Name the blood parasite species.
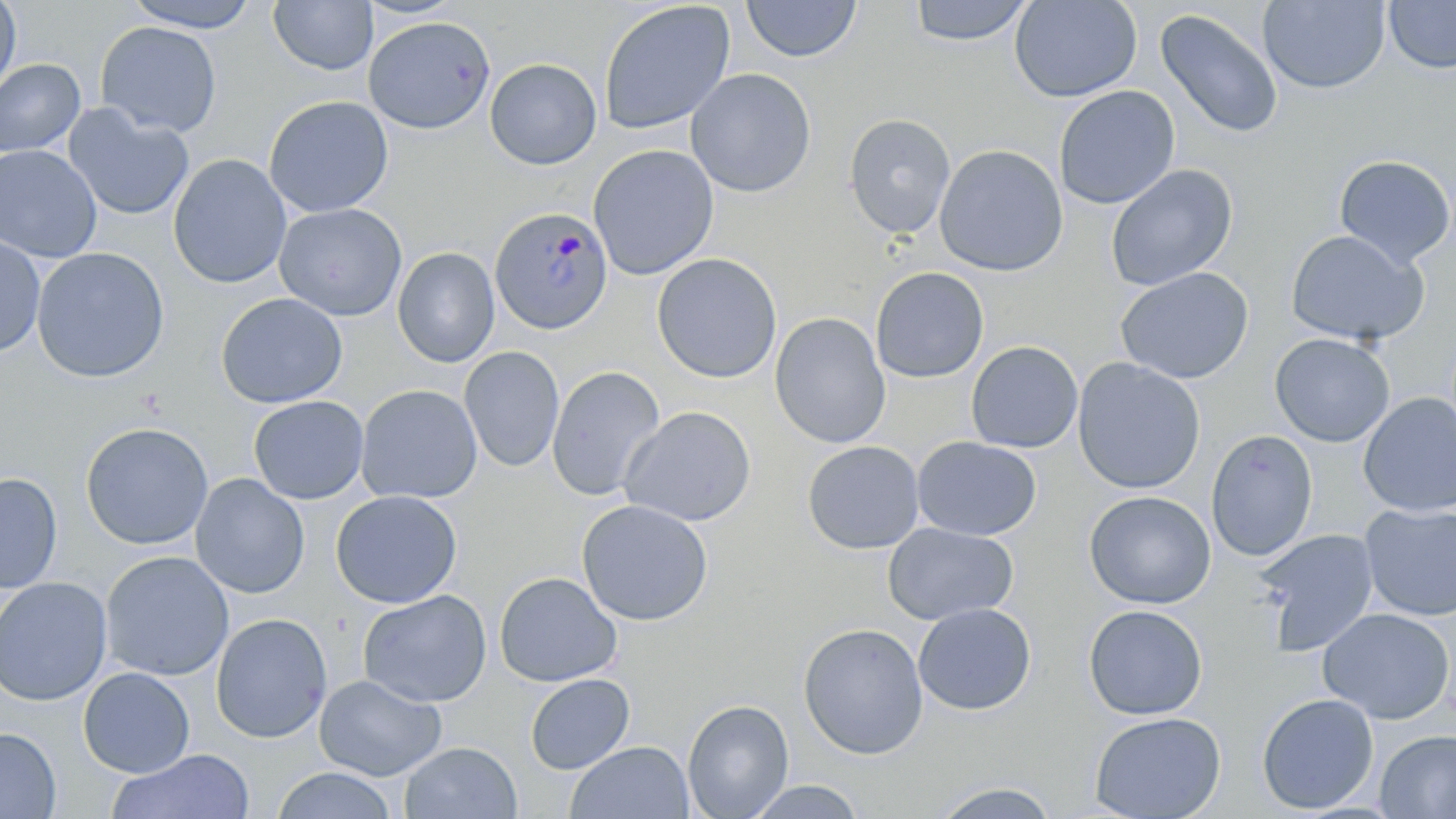

Plasmodium malariae.

Summary:
  - Coordinate format: approximate bounding boxes as [x1, y1, x2, y2] in pixels
  - Plasmodium malariae-infected red blood cell locations: [489, 207, 614, 336]
  - Uninfected red blood cell locations: [0, 0, 21, 97], [123, 0, 260, 31], [268, 0, 378, 76], [741, 0, 861, 63], [907, 0, 1034, 47], [1009, 0, 1142, 103], [598, 1, 736, 135], [1258, 1, 1391, 95], [1384, 1, 1456, 74], [1155, 8, 1284, 140], [362, 16, 495, 134], [95, 21, 222, 137], [0, 58, 85, 157], [485, 58, 602, 170], [685, 68, 817, 198], [1054, 85, 1180, 209], [264, 95, 394, 217], [63, 104, 195, 221], [843, 113, 956, 239], [0, 144, 102, 262], [588, 144, 719, 280], [934, 144, 1069, 276], [168, 154, 291, 289], [1334, 155, 1456, 268], [1105, 164, 1238, 291], [273, 203, 408, 321], [1285, 229, 1428, 346], [0, 235, 45, 357], [392, 246, 500, 368], [32, 247, 169, 382], [651, 253, 782, 383], [870, 266, 989, 383], [1115, 267, 1254, 384], [215, 292, 348, 409], [770, 312, 891, 448], [1269, 333, 1395, 447], [965, 341, 1083, 453], [459, 346, 564, 472], [1072, 358, 1206, 494], [547, 365, 665, 501], [356, 384, 483, 504], [1358, 393, 1456, 517], [248, 396, 369, 504], [619, 406, 757, 526], [80, 422, 214, 550], [1205, 429, 1318, 561], [912, 436, 1042, 542], [802, 441, 925, 554], [0, 473, 63, 593], [190, 474, 309, 598], [330, 490, 463, 608], [1083, 490, 1216, 609], [576, 499, 713, 627], [1360, 503, 1456, 621], [882, 522, 1018, 626], [1254, 529, 1380, 656], [100, 551, 234, 681], [494, 571, 622, 687], [0, 577, 113, 705], [357, 589, 492, 707], [913, 603, 1037, 716], [1083, 604, 1208, 720], [1317, 607, 1455, 724], [210, 613, 332, 744], [797, 622, 929, 759], [78, 667, 195, 777], [525, 673, 635, 774], [314, 674, 447, 781], [1256, 693, 1379, 814], [682, 699, 794, 818], [1089, 711, 1226, 819], [0, 727, 61, 819], [1375, 729, 1456, 818], [566, 740, 694, 819], [399, 742, 522, 819], [105, 748, 255, 819], [270, 767, 399, 819], [743, 780, 866, 818], [928, 780, 1062, 818]
  - Magnification: 1000x
  - Modality: optical microscopy
  - Field of view: one of a larger specimen
  - Stain: May-Grünwald-Giemsa
  - Image size: 1456×819 pixels
  - Preparation: thin blood smear